Give the extent of all uninfected red blood cells.
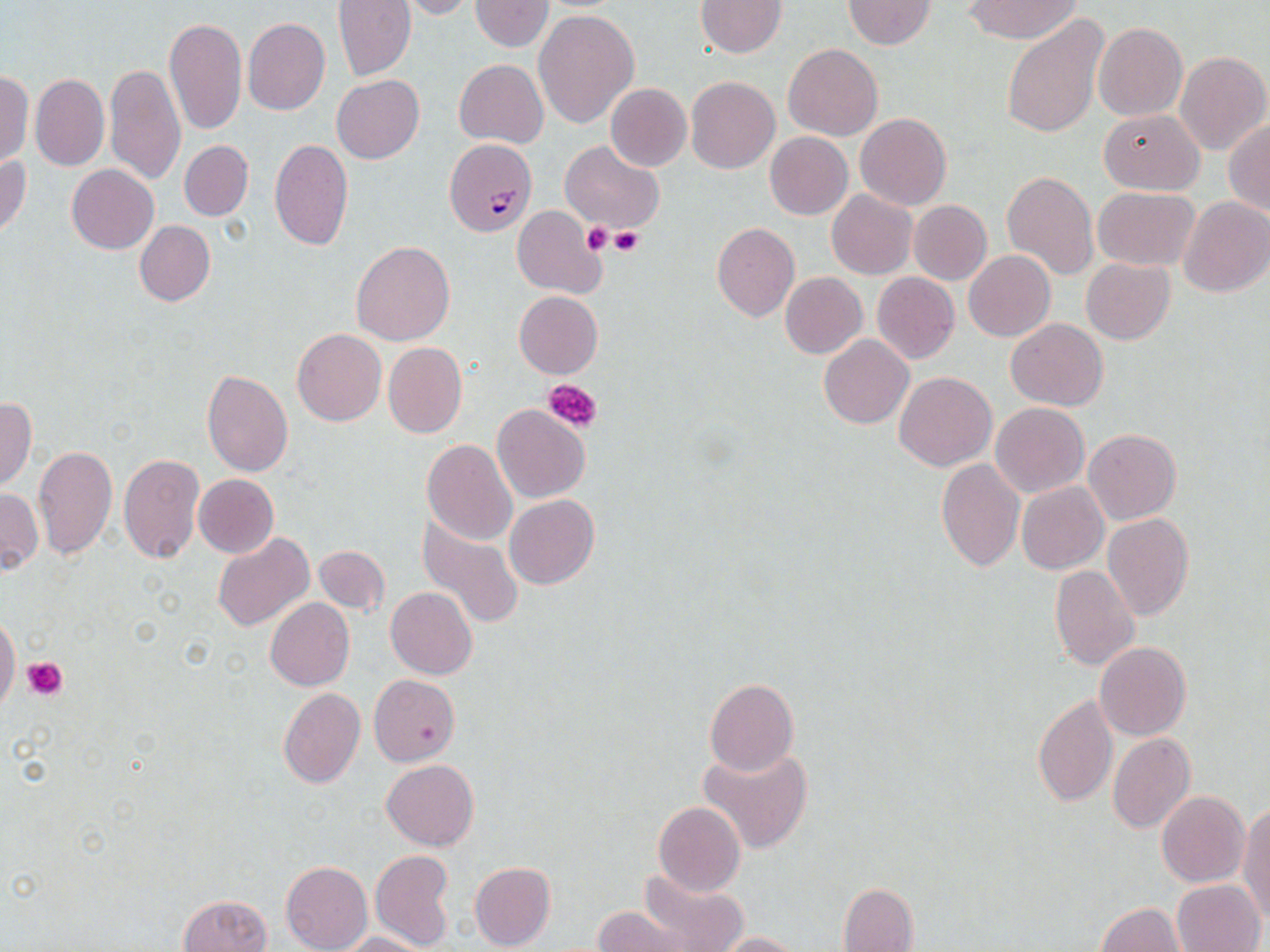

Approximate bounding boxes as [x1, y1, x2, y2] in pixels.
Uninfected red blood cells: [394, 0, 478, 20], [469, 0, 555, 51], [696, 0, 786, 57], [965, 0, 1080, 43], [331, 1, 416, 82], [842, 1, 935, 49], [533, 8, 639, 129], [1002, 14, 1108, 140], [164, 17, 247, 136], [243, 17, 330, 115], [1093, 22, 1187, 121], [783, 43, 882, 140], [1174, 50, 1270, 156], [454, 58, 548, 148], [105, 62, 184, 186], [0, 70, 33, 166], [31, 73, 109, 171], [331, 75, 424, 164], [686, 76, 780, 173], [605, 83, 692, 170], [1098, 110, 1204, 194], [855, 113, 951, 210], [1224, 119, 1270, 217], [764, 131, 853, 219], [269, 139, 353, 251], [179, 140, 253, 221], [558, 140, 665, 233], [0, 154, 31, 239], [66, 164, 158, 253], [1003, 169, 1099, 282], [1093, 186, 1200, 270], [827, 189, 918, 280], [1178, 196, 1270, 298], [909, 200, 991, 285], [511, 207, 605, 298], [134, 220, 215, 306], [712, 223, 799, 322], [351, 240, 455, 346], [964, 250, 1055, 341], [1081, 258, 1175, 344], [780, 271, 867, 358], [872, 273, 959, 363], [514, 291, 602, 378], [1005, 319, 1108, 410], [293, 329, 386, 426], [818, 336, 914, 429], [382, 343, 466, 438], [202, 370, 293, 477], [895, 371, 996, 470], [0, 397, 37, 491], [991, 402, 1089, 497], [493, 405, 590, 503], [1084, 428, 1181, 524], [422, 439, 518, 546], [34, 445, 116, 559], [118, 453, 205, 564], [935, 458, 1024, 572], [192, 474, 278, 558], [1017, 481, 1108, 574], [1, 487, 41, 575], [504, 495, 599, 590], [416, 513, 525, 629], [1103, 515, 1194, 620], [211, 532, 314, 631], [314, 545, 388, 617], [1048, 565, 1140, 672], [386, 586, 477, 679], [265, 598, 354, 691], [0, 615, 20, 713], [1095, 643, 1191, 741], [369, 673, 460, 766], [704, 678, 798, 775], [277, 688, 365, 789], [1032, 693, 1119, 809], [1107, 732, 1195, 833], [698, 746, 812, 854], [382, 759, 479, 852], [1157, 790, 1249, 887], [653, 802, 746, 897], [1238, 805, 1270, 920], [369, 850, 455, 950], [281, 860, 372, 952], [469, 861, 556, 951], [638, 866, 747, 952], [1171, 879, 1264, 952], [838, 882, 919, 951], [178, 893, 273, 952], [1095, 903, 1185, 952], [593, 905, 689, 952], [339, 931, 430, 952], [709, 932, 802, 951].

Platelet locations: [582, 222, 616, 256], [612, 229, 643, 255], [544, 378, 602, 434], [23, 656, 66, 700]. Plasmodium falciparum-infected red blood cell locations: [444, 138, 536, 237]. Slide-level diagnosis: Plasmodium falciparum. Thin blood film. Image is 1270×952 pixels. Single field of view. Captured at 1000x magnification. May-Grünwald-Giemsa-stained preparation. Light microscopy.